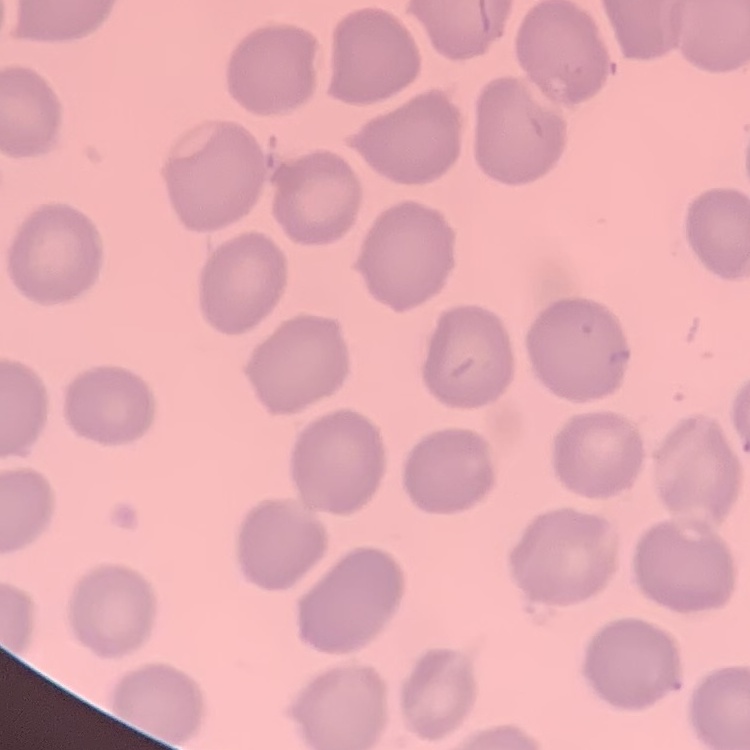

{
  "erythrocyte_morphology": "no rouleaux formation",
  "stain": "Field's or Giemsa",
  "image_type": "one tile cut from a larger photomicrograph",
  "preparation": "thin peripheral smear"
}